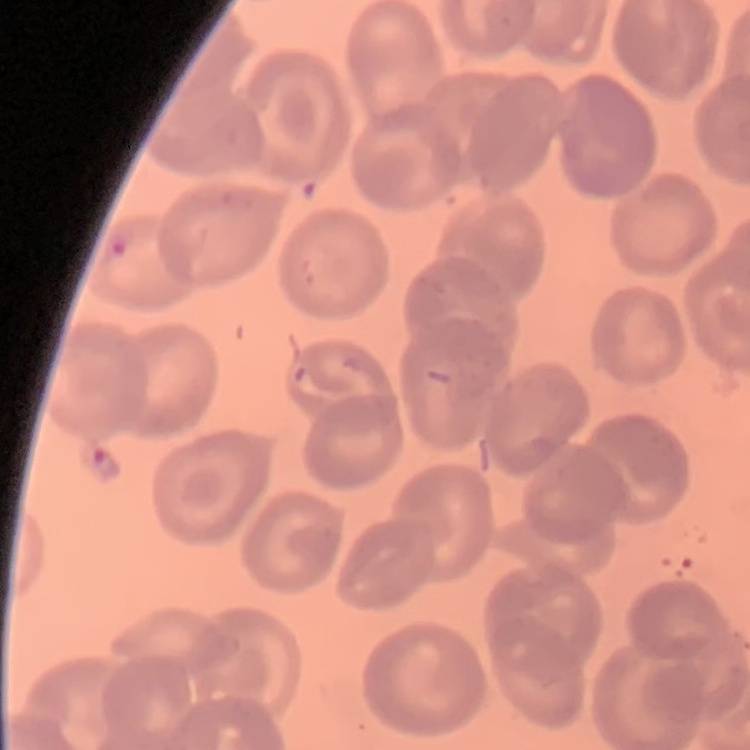

Summary:
  - Erythrocyte morphology: no rouleaux formation
  - Preparation: thin peripheral smear
  - Image type: square crop of a larger photomicrograph
  - Stain: Field's or Giemsa